Classify this cell by malaria status.
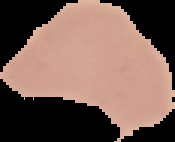

Uninfected.

image_type: segmented cell region on a black background
preparation: thin blood smear
image_size: 175×142 pixels